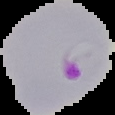 Malaria status: parasitized. Image is 115×115 pixels. Cell region segmented out of the field of view; the surrounding area is masked to black. From a thin blood smear.